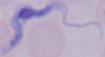
{
  "identification": "trypanosome",
  "magnification": "1000x",
  "modality": "photomicrograph"
}